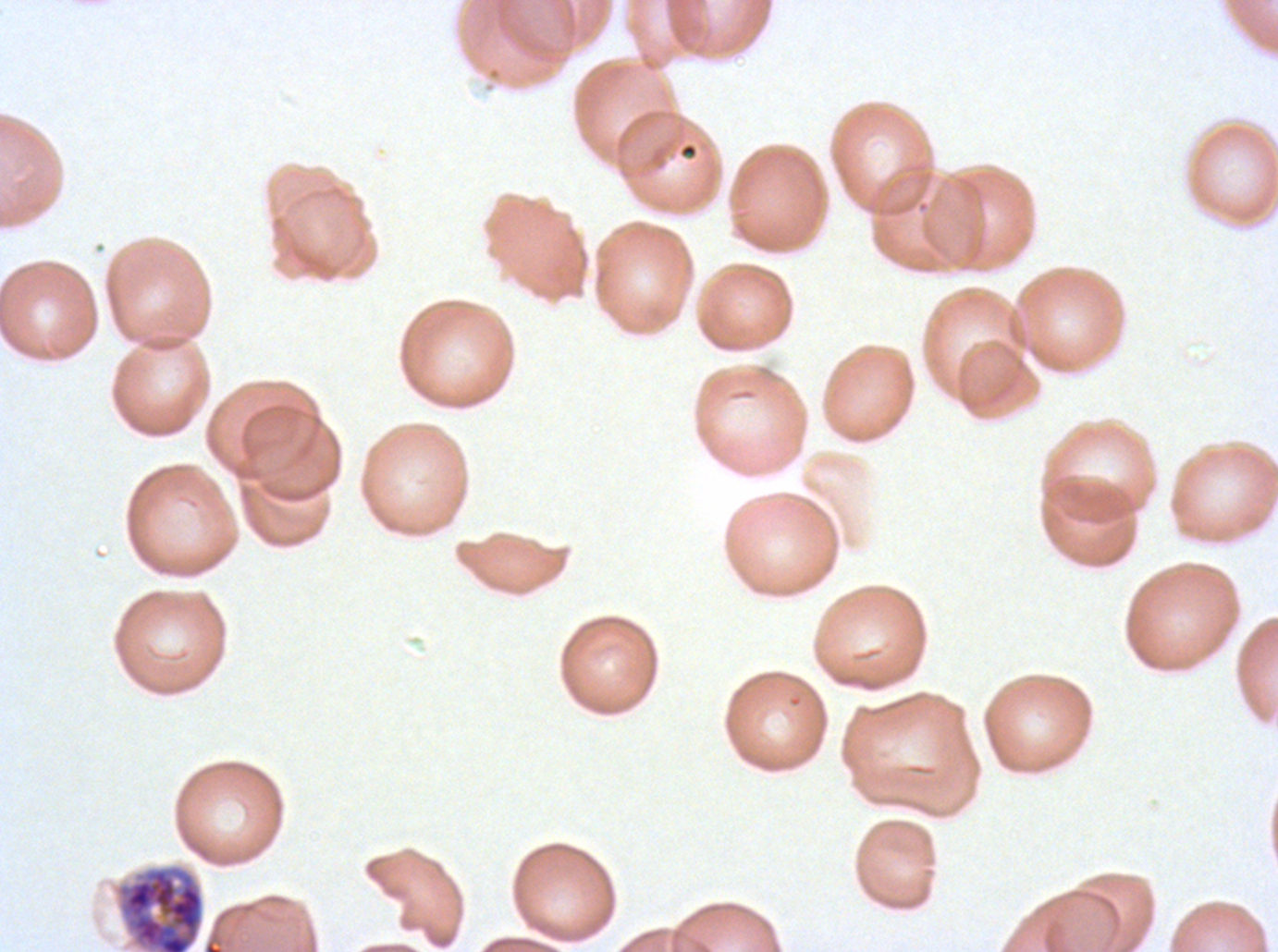

Approximate bounding boxes as [x1, y1, x2, y2] in pixels.
Summary:
  - Early schizont locations: [116, 864, 204, 951]
  - Stain: Giemsa
  - Preparation: thin blood film
  - Image size: 1278×952 pixels
  - Field of view: one sub-image of a larger composite
  - Specimen: ex-vivo Plasmodium falciparum culture from a patient in The Gambia, grown for 24 to 48 hours